Locate every Plasmodium parasite.
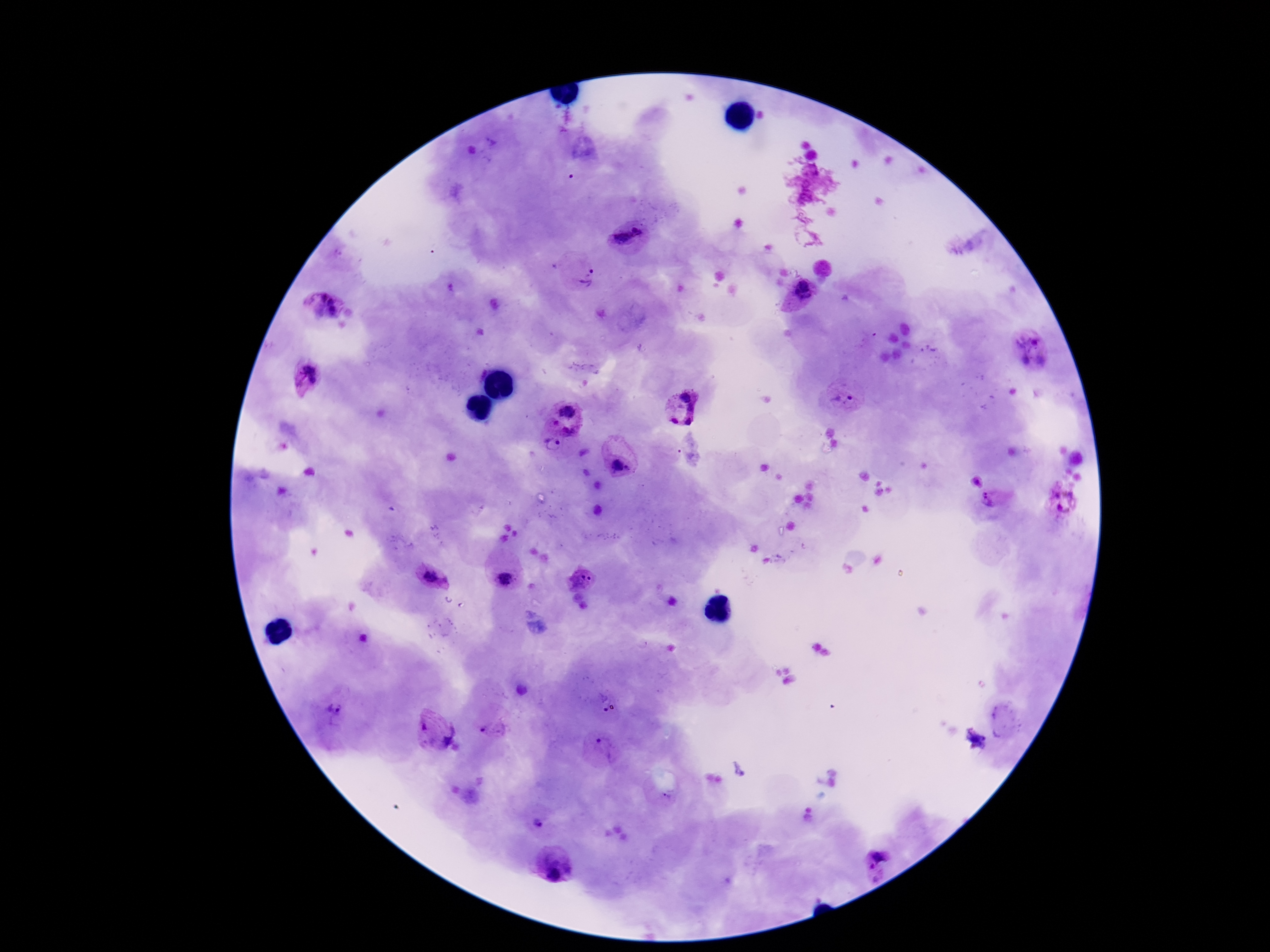
Approximate centers as {x, y} in pixels.
Plasmodium parasites: {638, 230}, {623, 237}, {586, 276}, {803, 290}, {321, 296}, {331, 301}, {334, 312}, {1036, 340}, {1024, 359}, {1040, 360}, {308, 378}, {843, 401}, {683, 409}, {568, 410}, {555, 422}, {571, 430}, {552, 444}, {621, 465}, {976, 480}, {1063, 499}, {994, 500}, {431, 577}, {505, 578}, {581, 580}, {335, 710}, {423, 727}, {486, 731}, {451, 736}, {599, 741}, {668, 794}, {538, 823}, {882, 855}, {871, 870}, {557, 872}.

{
  "field_of_view": "one from this slide",
  "preparation": "thick blood smear",
  "patient_malaria_status": "positive",
  "capture": "smartphone camera through the microscope eyepiece",
  "image_size": "1270×952 pixels",
  "stain": "Giemsa",
  "magnification": "100x"
}